Give the position of every malaria parasite.
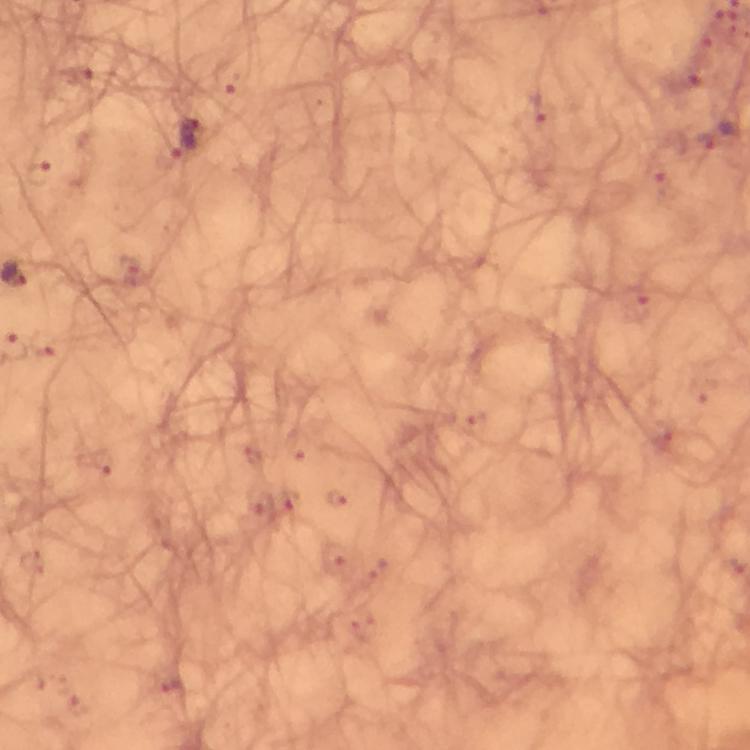

Approximate object centers, in pixels from the top-left corner.
Malaria parasites: (x=718, y=135), (x=185, y=138).

{
  "immersion_oil": "used",
  "cropped_from": "one field of view",
  "image_size": "750×750 pixels",
  "stain": "Giemsa",
  "magnification": "100x",
  "context": "from a diagnostic examination for malaria",
  "preparation": "thick smear",
  "capture": "smartphone photograph through a microscope"
}